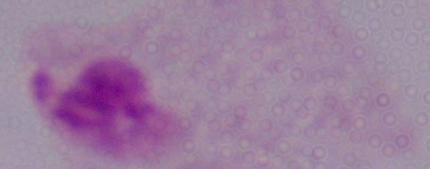 A trichomonad is shown. Captured at 1000x magnification. Photomicrograph.